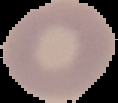
Summary:
  - Malaria status: uninfected
  - Image type: segmented cell region with the area outside set to black
  - Preparation: thin blood smear
  - Image size: 118×103 pixels